Classify this cell by malaria status.
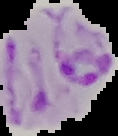

It is parasitized.

image type = segmented cell region with the area outside set to black
preparation = thin blood film
image size = 118×136 pixels